Classify this cell by malaria status.
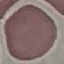
Uninfected.

Summary:
  - Preparation: thin blood smear
  - Image type: automatically extracted cell patch, resized to 64 × 64 pixels
  - Capture: smartphone through the microscope eyepiece
  - Stain: Giemsa